Classify this cell by malaria status.
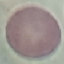

Uninfected.

Summary:
  - Image type: cell patch, automatically extracted from a larger field of view and resized to 64 × 64 pixels
  - Preparation: thin smear
  - Capture: smartphone through the microscope eyepiece
  - Stain: Giemsa